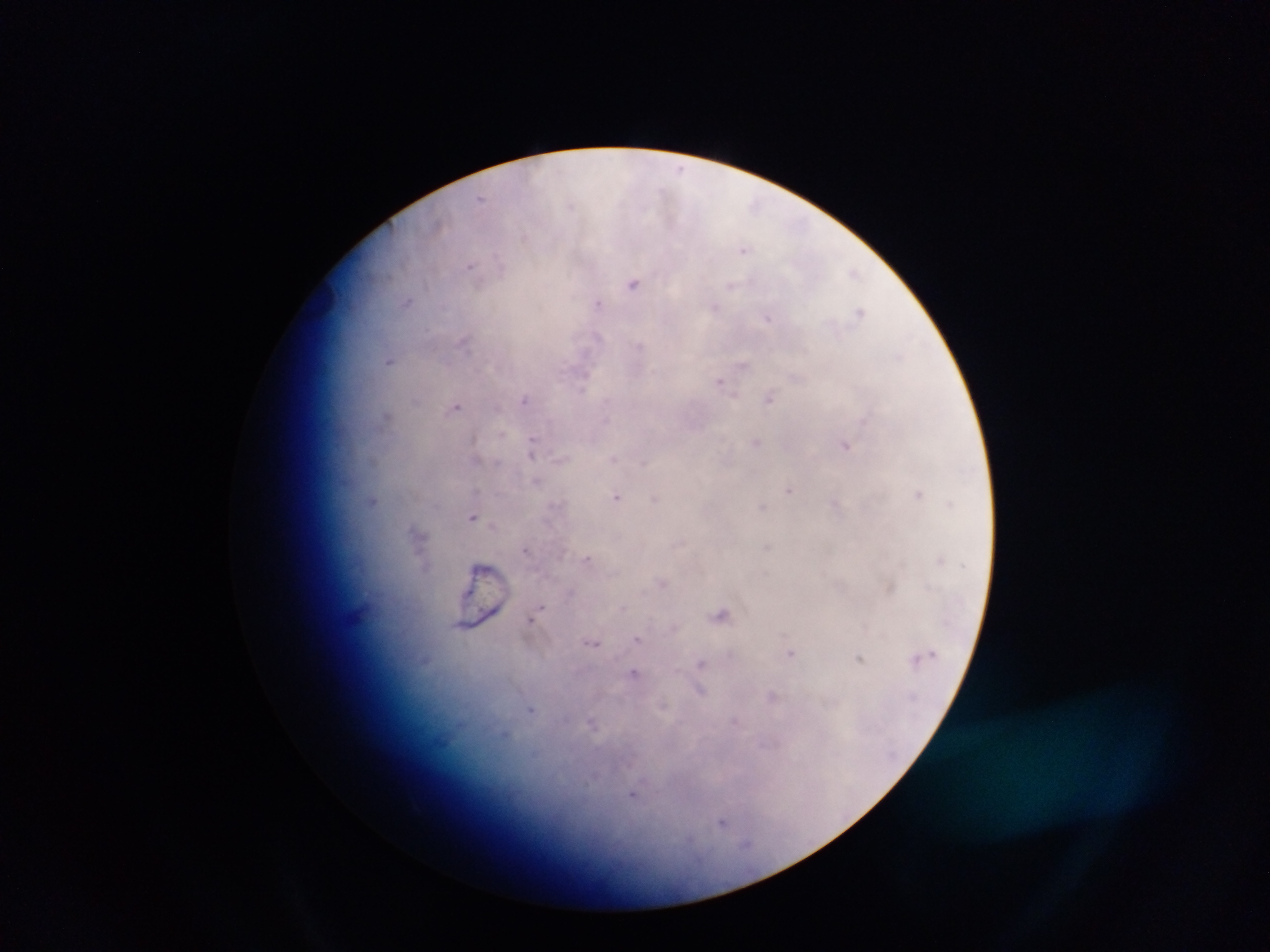

plasmodium_parasite_locations: 'approximate centers as {x, y} in pixels: {680, 168}, {480, 198}, {570, 204}, {754, 204}, {744, 250}, {470, 264}, {853, 272}, {633, 283}, {731, 286}, {408, 302}, {597, 302}, {715, 306}, {859, 311}, {768, 318}, {596, 335}, {463, 341}, {640, 346}, {900, 355}, {390, 360}, {743, 365}, {584, 376}, {795, 377}, {720, 381}, {769, 398}, {415, 399}, {524, 399}, {457, 407}, {386, 416}, {502, 433}, {756, 441}, {532, 446}, {847, 446}, {532, 455}, {613, 458}, {475, 459}, {372, 460}, {642, 463}, {536, 481}, {790, 490}, {919, 494}, {616, 497}, {655, 498}, {372, 500}, {950, 504}, {762, 506}, {836, 506}, {473, 517}, {415, 530}, {767, 547}, {525, 550}, {587, 558}, {940, 559}, {662, 583}, {890, 588}, {538, 610}, {721, 614}, {532, 619}, {637, 638}, {593, 643}, {791, 653}, {859, 658}, {915, 659}, {700, 662}, {633, 673}, {699, 690}, {771, 696}, {531, 709}, {734, 721}, {592, 723}, {505, 734}, {633, 794}, {722, 821}, {746, 844}'
preparation: thick blood smear
country: Ghana
capture: mobile-phone photograph through a microscope
field_of_view: single
image_size: 1270×952 pixels